Name the cell type shown.
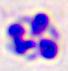

This is a leukocyte.

modality = photomicrograph
magnification = 400x